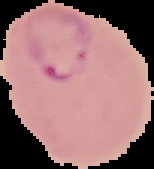
Summary:
  - Preparation: thin blood smear
  - Image size: 154×169 pixels
  - Image type: segmented cell region on a black background
  - Result: Plasmodium parasites detected